Outline each blood parasite and name the species.
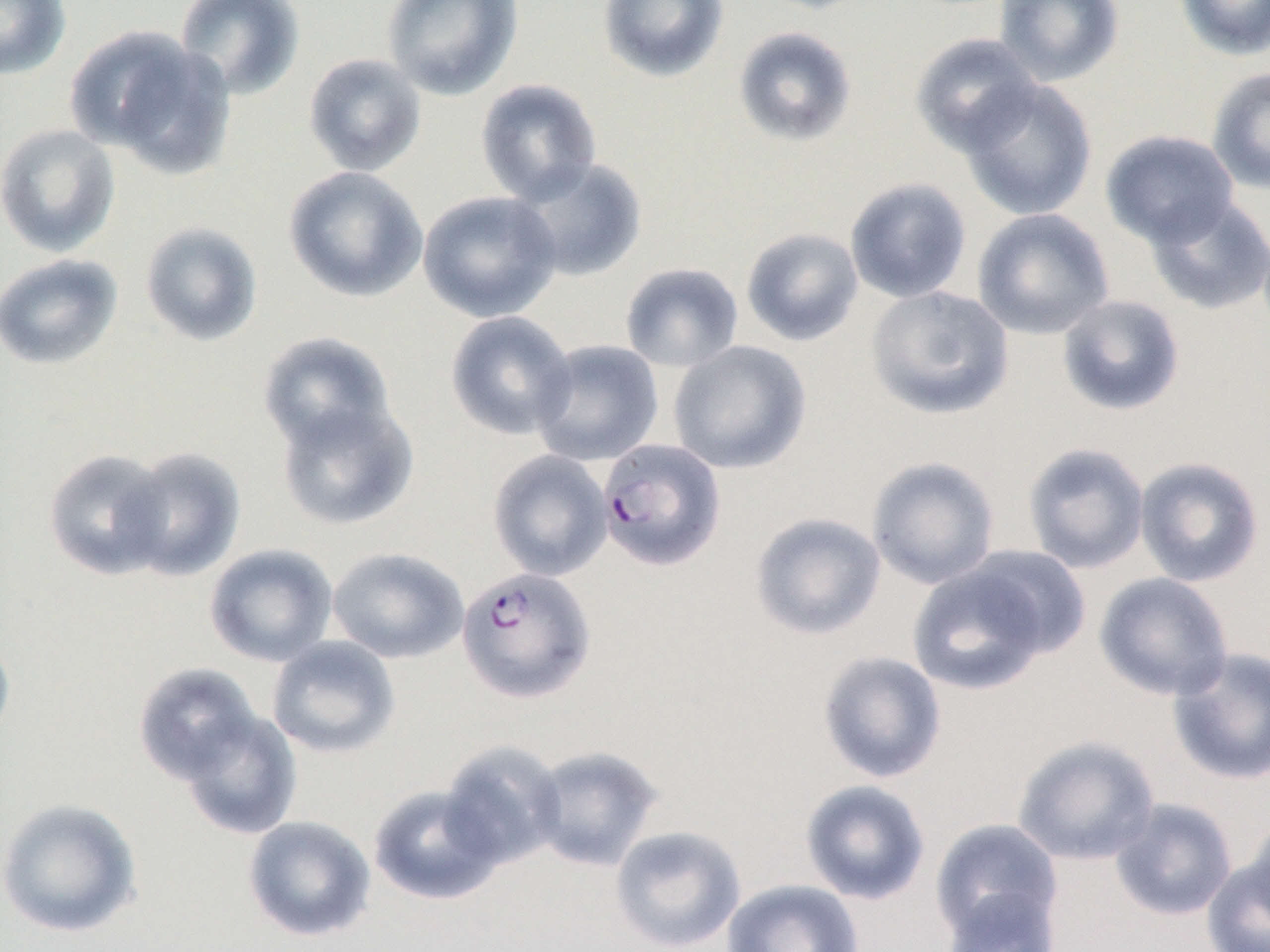
Approximate bounding boxes as (x1,y1)-(x2,y2) corner pairs in pixels.
Plasmodium falciparum-infected red blood cells: (597,438)-(726,570), (457,566)-(596,703).
No Plasmodium ovale, Plasmodium malariae, Plasmodium vivax, Babesia divergens, or Trypanosoma brucei observed.

{
  "slide_level_diagnosis": "Plasmodium falciparum",
  "magnification": "1000x",
  "modality": "optical microscopy",
  "preparation": "thin blood smear",
  "uninfected_red_blood_cell_locations": "approximate bounding boxes as (x1,y1)-(x2,y2) corner pairs in pixels: (0,0)-(71,80), (174,0)-(306,101), (381,0)-(523,100), (598,0)-(729,83), (753,0)-(876,15), (994,0)-(1125,87), (1174,0)-(1270,60), (65,24)-(234,177), (733,25)-(858,147), (910,33)-(1042,156), (303,53)-(428,177), (1206,67)-(1270,194), (957,77)-(1098,221), (475,79)-(602,205), (0,123)-(121,257), (1100,130)-(1240,249), (510,157)-(648,282), (283,166)-(428,303), (844,178)-(972,303), (418,190)-(563,323), (1145,195)-(1270,315), (972,207)-(1114,340), (140,221)-(264,347), (741,228)-(863,346), (0,254)-(124,371), (620,262)-(744,372), (866,285)-(1015,421), (1056,294)-(1185,416), (445,311)-(577,441), (257,331)-(398,453), (531,339)-(664,466), (668,340)-(811,475), (274,396)-(419,531), (1022,442)-(1150,574), (120,445)-(248,581), (44,448)-(174,580), (487,449)-(613,581), (866,456)-(1001,590), (1134,456)-(1265,588), (750,512)-(886,640), (204,544)-(338,667), (956,545)-(1091,667), (327,547)-(469,664), (907,557)-(1060,696), (1094,572)-(1235,701), (0,629)-(16,750), (266,636)-(401,758), (1167,646)-(1270,786), (817,650)-(947,784), (132,663)-(263,786), (176,707)-(303,840), (1013,736)-(1160,865), (438,740)-(567,870), (529,745)-(665,872), (800,779)-(931,905), (368,783)-(506,905), (0,797)-(143,937), (1110,798)-(1237,921), (1245,813)-(1270,933), (243,815)-(377,942), (930,818)-(1063,945), (609,825)-(747,951), (1201,854)-(1270,952), (722,879)-(865,952), (941,887)-(1061,952)",
  "field_of_view": "single",
  "image_size": "1270×952 pixels"
}